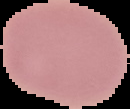

preparation = thin blood smear
image type = cell region segmented out of the field of view; surrounding area masked to black
malaria status = uninfected
image size = 130×109 pixels